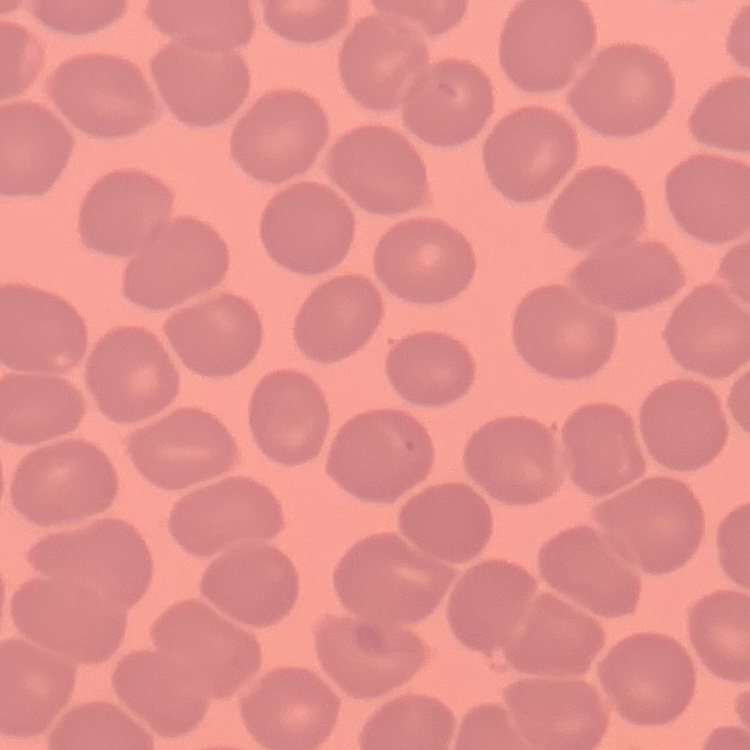 The erythrocytes exhibit no rouleaux formation. Thin blood film. Stained with either Field's or Giemsa. Square crop of a larger photomicrograph.